Assess this cell for malaria.
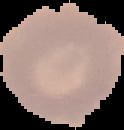

Uninfected.

Image is 124×130 pixels. Cell region segmented out of the field of view; the surrounding area is masked to black. From a thin blood smear.